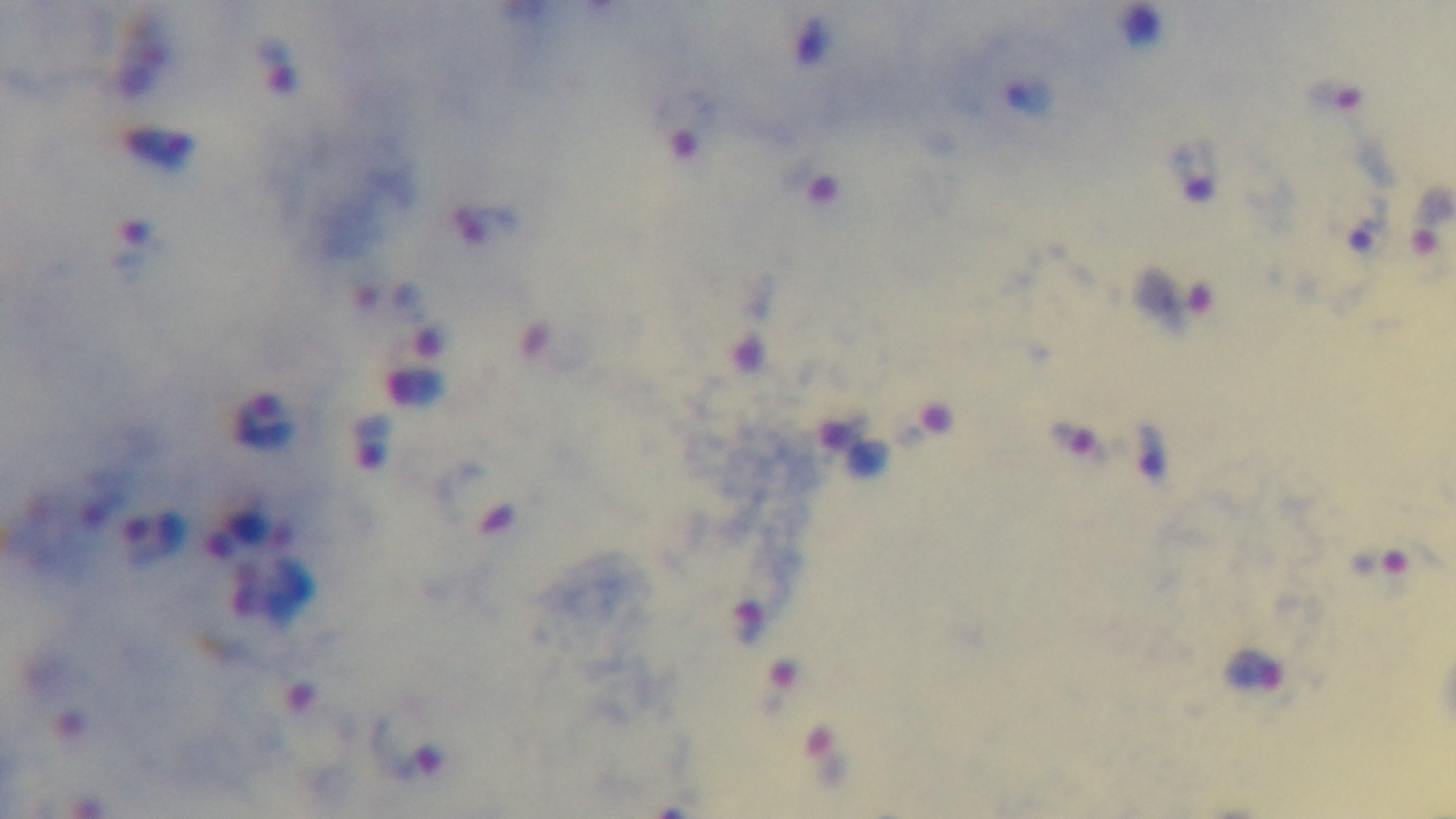

Preparation: thick smear. Giemsa stain. Photomicrograph. Malaria status: positive. 100x oil-immersion objective. One field from the slide. Captured with a mounted 4K digital camera.